Give the preparation type.
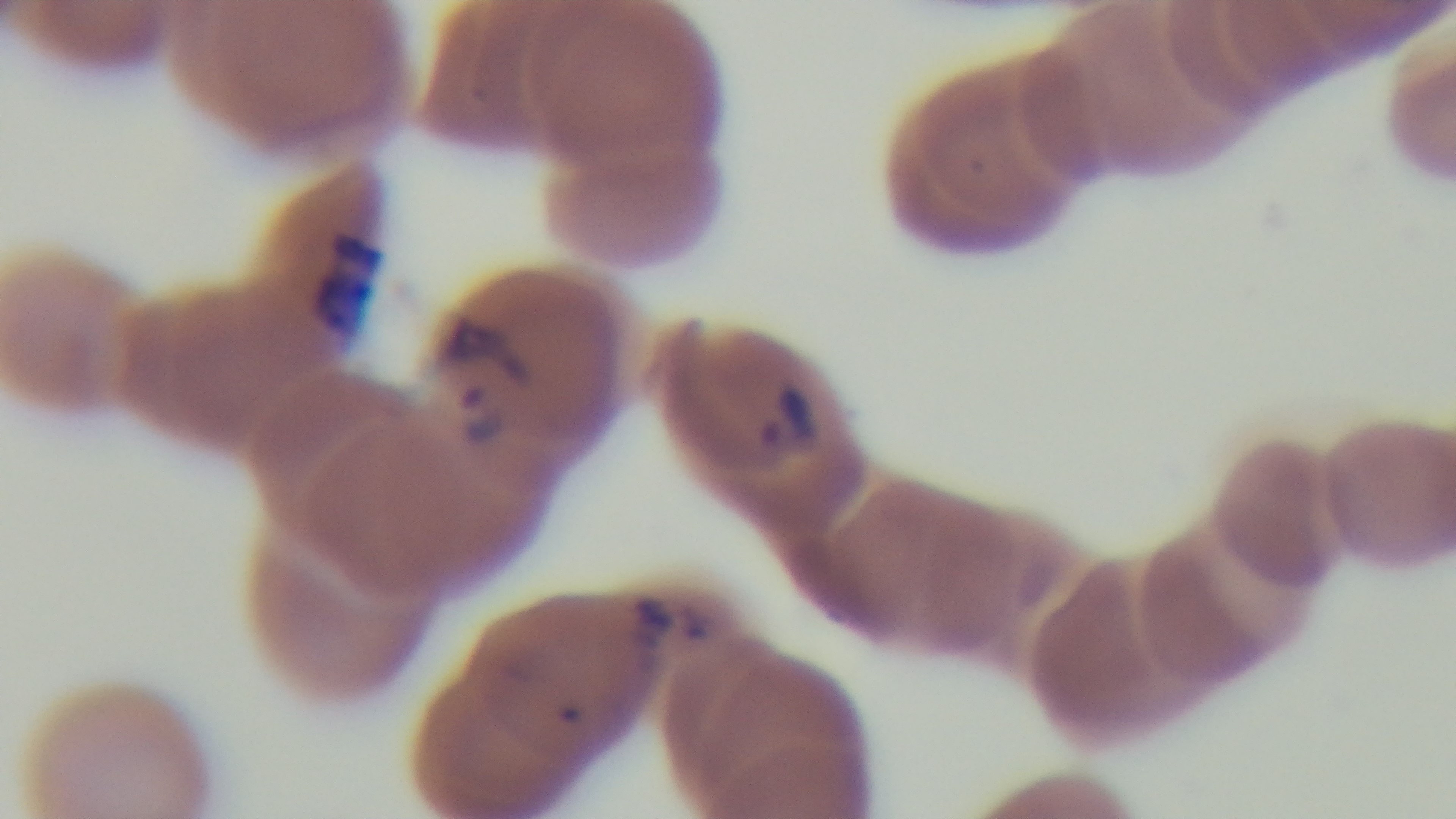

Thin.

modality: light microscopy
field_of_view: one from the slide
objective: 100x oil immersion
capture: mounted 4K digital camera
stain: Giemsa
malaria_status: positive